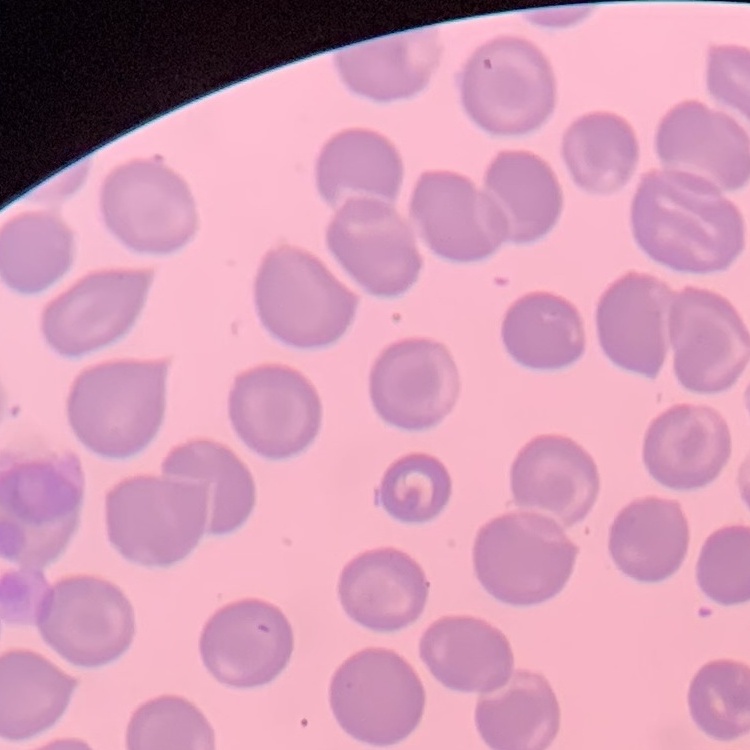
The erythrocytes show no rouleaux formation. Thin blood smear. One tile cut from a larger photomicrograph. Field's or Giemsa stain.